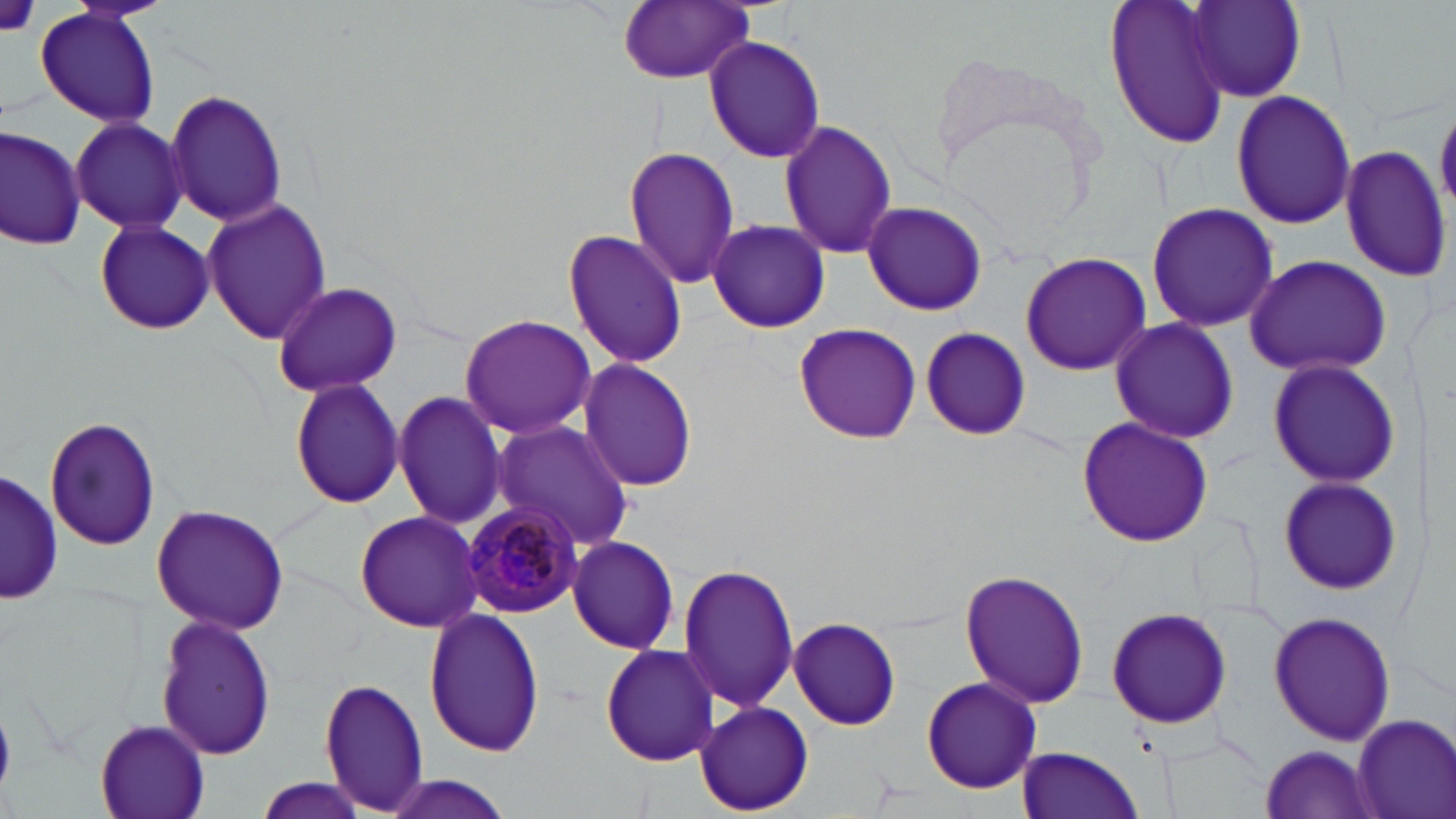
Summary:
  - Coordinate format: approximate bounding boxes as (x1, y1, x2, y2) in pixels
  - Platelet locations: (1, 0, 40, 38)
  - Uninfected red blood cell locations: (1103, 0, 1236, 150), (1185, 0, 1306, 102), (616, 1, 757, 83), (34, 6, 162, 130), (703, 34, 826, 164), (163, 88, 288, 226), (1231, 90, 1356, 230), (70, 117, 190, 236), (777, 120, 898, 260), (0, 124, 84, 249), (1341, 145, 1451, 281), (624, 146, 740, 288), (199, 198, 331, 346), (860, 199, 988, 316), (1143, 202, 1280, 333), (707, 218, 831, 335), (92, 219, 216, 336), (561, 229, 688, 368), (1020, 249, 1152, 376), (1242, 253, 1393, 379), (270, 279, 403, 398), (459, 313, 596, 439), (1107, 318, 1241, 445), (792, 320, 920, 446), (917, 327, 1029, 440), (1266, 356, 1400, 490), (575, 359, 700, 492), (288, 377, 406, 508), (392, 389, 509, 529), (1075, 416, 1214, 548), (44, 417, 160, 553), (489, 420, 635, 551), (3, 467, 61, 608), (1277, 473, 1401, 596), (151, 503, 292, 635), (352, 510, 483, 633), (566, 534, 681, 655), (678, 563, 799, 712), (958, 568, 1092, 709), (1105, 603, 1234, 730), (422, 607, 547, 759), (1267, 608, 1396, 748), (155, 612, 278, 762), (787, 616, 902, 730), (599, 642, 720, 766), (920, 676, 1043, 794), (319, 680, 430, 812), (695, 701, 813, 815), (1351, 712, 1456, 819), (93, 720, 211, 819), (1016, 745, 1145, 819), (1258, 746, 1382, 817), (249, 777, 372, 819), (374, 777, 518, 819)
  - Plasmodium malariae-infected red blood cell locations: (460, 502, 585, 617)
  - Slide-level diagnosis: Plasmodium malariae
  - Preparation: thin blood smear
  - Stain: May-Grünwald-Giemsa
  - Image size: 1456×819 pixels
  - Modality: light microscopy
  - Field of view: one of a larger specimen
  - Magnification: 1000x